Assess the morphology of the erythrocytes.
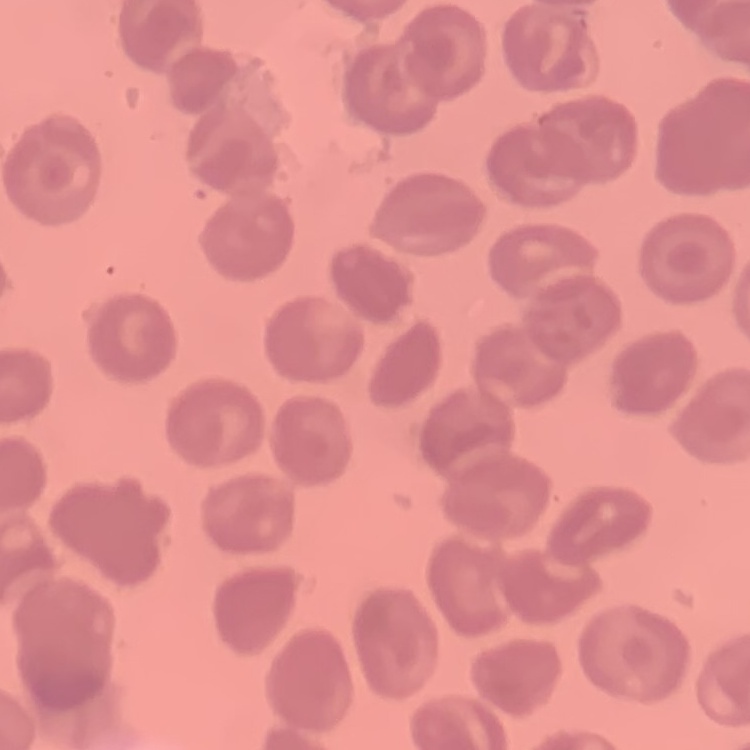
No rouleaux formation.

Summary:
  - Stain: Field's or Giemsa
  - Image type: one tile cut from a larger photomicrograph
  - Preparation: thin blood film